Identify the parasite.
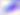
This is Toxoplasma gondii.

Summary:
  - Magnification: 400x
  - Modality: photomicrograph